Classify this cell by malaria status.
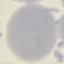

It is uninfected.

Giemsa stain. Thin blood smear. Cell patch, automatically extracted from a larger field of view and resized to 64 × 64 pixels. Acquired by smartphone through the microscope eyepiece.